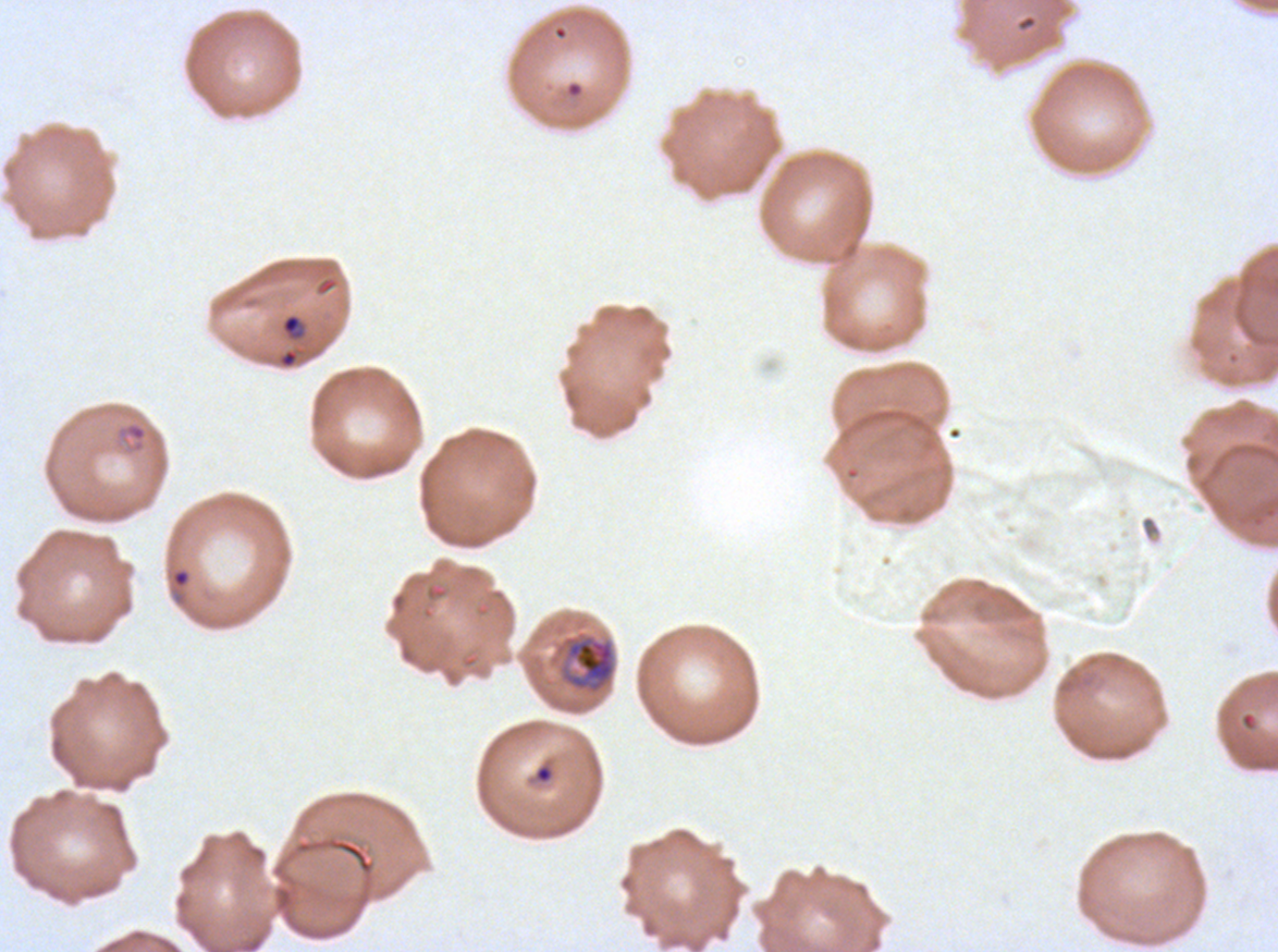 Approximate bounding boxes as (x1, y1, x2, y2) in pixels. Mid trophozoite locations: (554, 630, 617, 696). Ring locations: (280, 312, 305, 341), (116, 421, 149, 454), (171, 568, 190, 588), (534, 763, 554, 785). Ex-vivo P. falciparum culture from a patient in The Gambia, grown for 24 to 48 hours. One sub-image of a larger composite. Life-cycle stages observed: ring, mid trophozoite. Image is 1278×952 pixels. Thin blood smear. Giemsa-stained preparation.